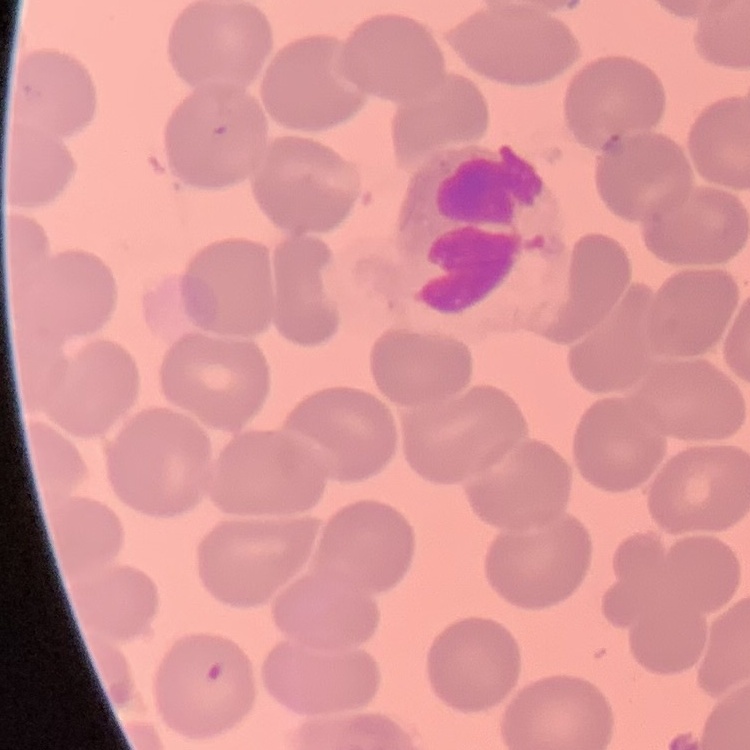

Summary:
  - Erythrocyte morphology: no rouleaux formation
  - Preparation: thin peripheral smear
  - Image type: square crop of a larger photomicrograph
  - Stain: Field's or Giemsa